Give the extent of all uninfected red blood cells.
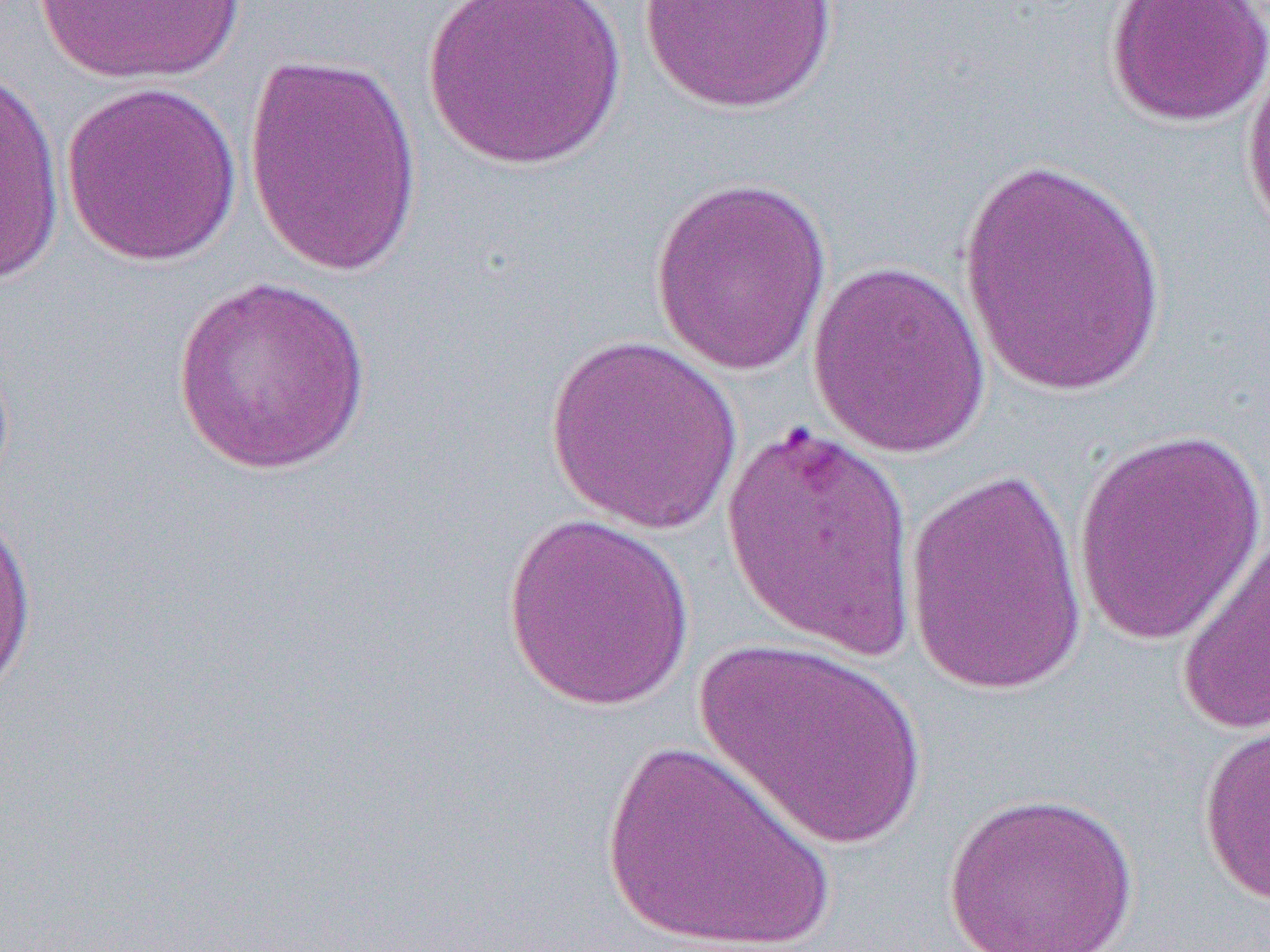
Approximate bounding boxes as [x1, y1, x2, y2] in pixels.
Uninfected red blood cells: [30, 0, 251, 86], [422, 0, 629, 171], [638, 0, 841, 114], [1104, 0, 1270, 128], [1241, 42, 1270, 257], [242, 52, 423, 277], [1, 68, 67, 286], [60, 80, 244, 267], [957, 153, 1167, 399], [648, 176, 834, 376], [806, 259, 992, 458], [172, 274, 373, 476], [543, 335, 744, 535], [717, 418, 920, 666], [1071, 428, 1268, 647], [902, 467, 1088, 694], [0, 502, 39, 707], [501, 514, 695, 711], [1174, 526, 1270, 736], [693, 633, 929, 851], [1196, 714, 1270, 907], [599, 738, 837, 951], [942, 790, 1140, 952].

{
  "slide_level_diagnosis": "Plasmodium falciparum",
  "preparation": "thin blood film",
  "modality": "optical microscopy",
  "magnification": "1000x",
  "field_of_view": "single",
  "image_size": "1270×952 pixels"
}